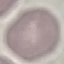 Malaria status: uninfected. Acquired by smartphone through the microscope eyepiece. Thin blood smear. Giemsa stain. Cell patch, automatically extracted from a larger field of view and resized to 64 × 64 pixels.